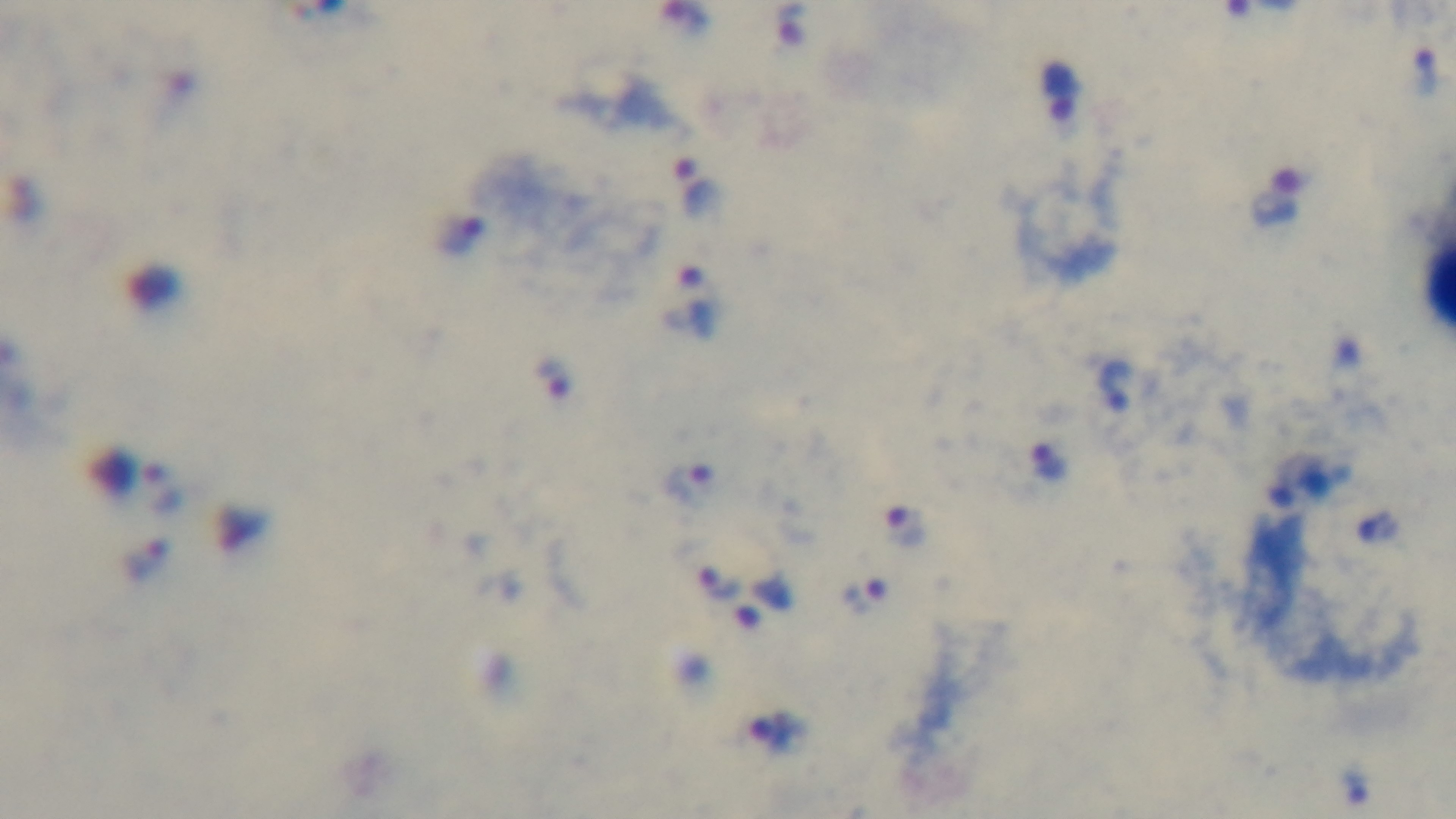
Summary:
  - Modality: light microscopy
  - Preparation: thick smear
  - Objective: 100x oil immersion
  - Capture: mounted 4K digital camera
  - Malaria status: positive
  - Field of view: single
  - Stain: Giemsa